Identify the cell.
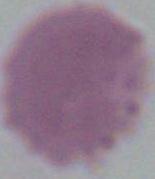
An erythrocyte.

Summary:
  - Magnification: 1000x
  - Modality: micrograph